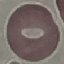

result = no malaria parasites seen
image type = automatically extracted cell patch, resized to 64 × 64 pixels
capture = smartphone camera at the microscope eyepiece
stain = Giemsa
preparation = thin smear